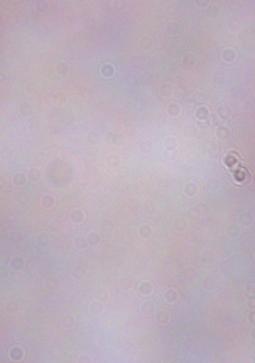
Summary:
  - Identification: trypanosome
  - Magnification: 1000x
  - Modality: micrograph